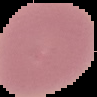

image size = 97×97 pixels
result = no Plasmodium parasites detected
image type = cell region segmented out of the field of view; surrounding area masked to black
preparation = thin blood film